Describe the morphology of the red blood cells.
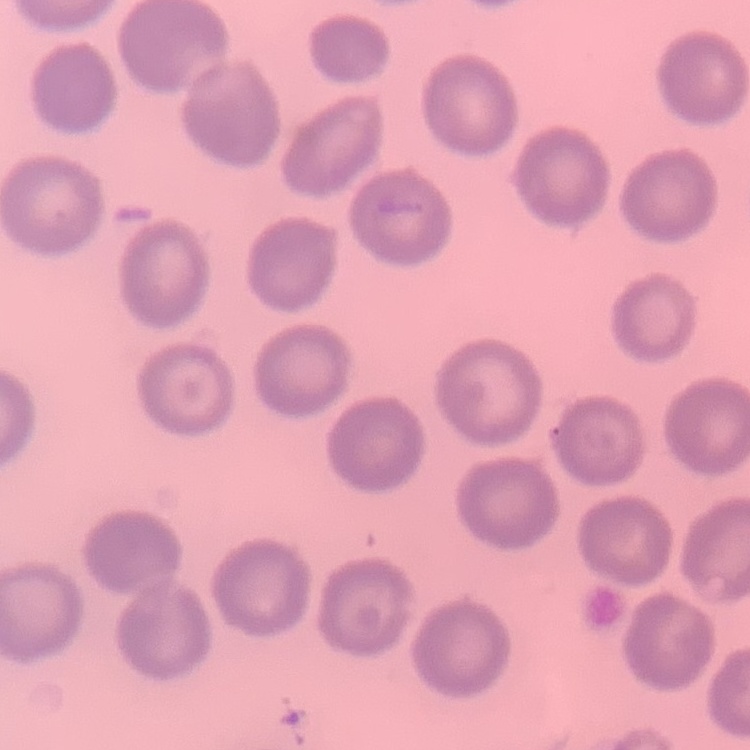
They show no rouleaux formation.

preparation = thin blood smear
image type = square crop of a larger photomicrograph
stain = Field's or Giemsa